Identify the parasite.
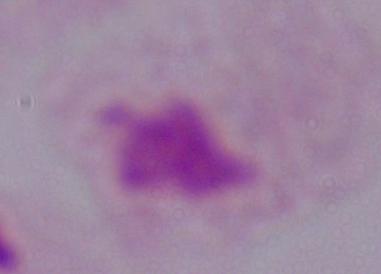

This is a trichomonad.

Summary:
  - Modality: micrograph
  - Magnification: 1000x